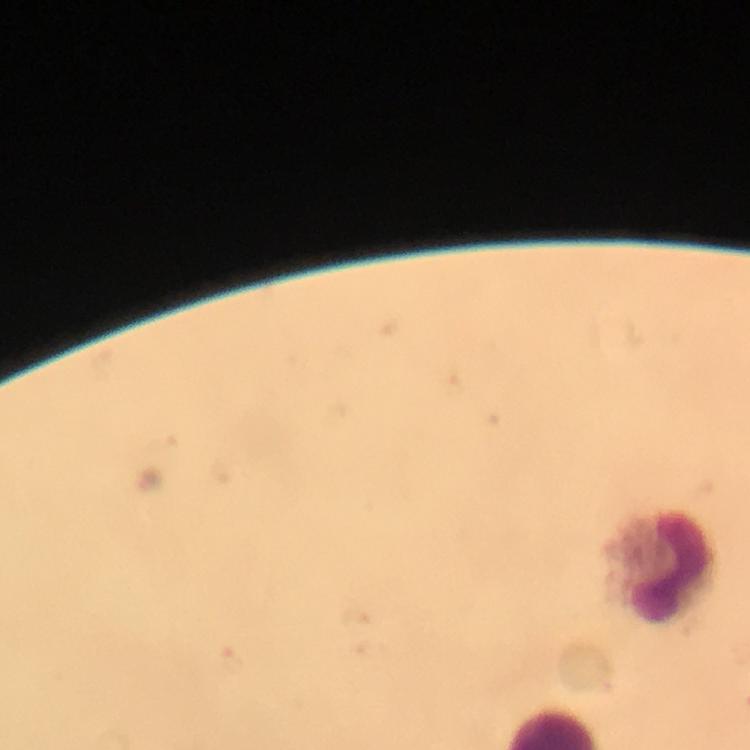

Approximate centers as (x, y) in pixels.
Summary:
  - Leukocyte locations: (663, 567)
  - Context: from a malaria diagnostic workup
  - Stain: Giemsa
  - Immersion oil: used
  - Preparation: thick blood film
  - Cropped from: one field of view
  - Magnification: 100x
  - Capture: smartphone mounted on the microscope
  - Image size: 750×750 pixels
  - Plasmodium parasites: none detected